Point out each leukocyte.
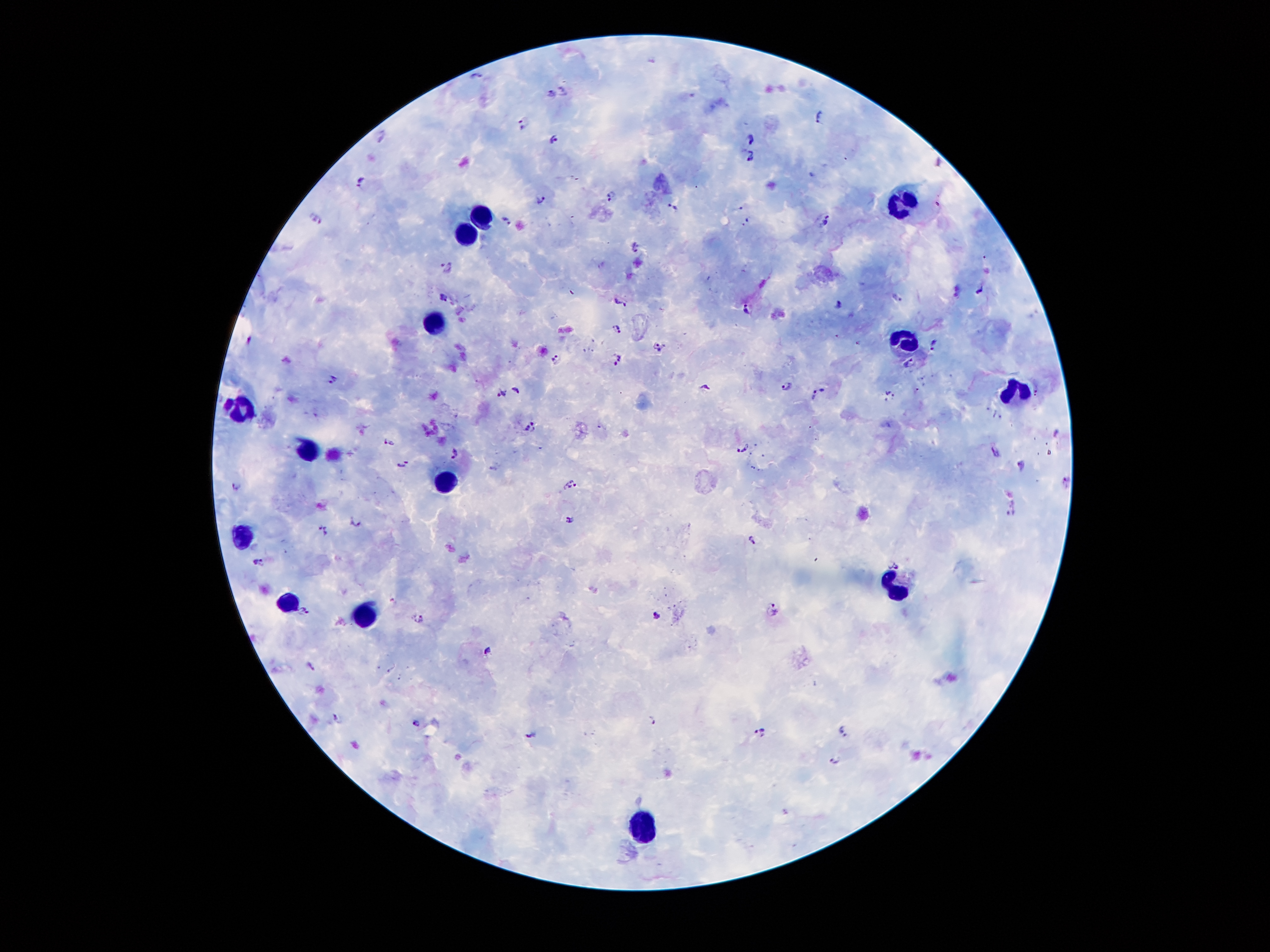
Approximate centers as (x, y) in pixels.
Leukocytes: (901, 209), (485, 221), (472, 231), (435, 326), (904, 345), (1019, 393), (240, 411), (308, 449), (442, 484), (243, 541), (902, 589), (293, 604), (367, 615), (651, 822).

Summary:
  - Plasmodium parasite locations: (654, 60), (477, 76), (564, 90), (552, 94), (817, 115), (522, 124), (381, 133), (750, 138), (553, 139), (751, 155), (359, 182), (612, 195), (540, 200), (672, 207), (739, 210), (507, 220), (316, 221), (826, 221), (745, 224), (635, 247), (447, 266), (978, 290), (572, 292), (443, 297), (898, 297), (620, 302), (838, 305), (746, 309), (618, 329), (837, 336), (250, 339), (859, 343), (934, 344), (658, 347), (618, 358), (556, 359), (910, 364), (333, 379), (786, 386), (707, 387), (515, 389), (499, 392), (817, 393), (890, 397), (531, 427), (1057, 433), (388, 443), (743, 448), (997, 453), (454, 454), (404, 463), (1022, 464), (1066, 480), (571, 485), (235, 486), (1011, 511), (569, 518), (355, 522), (324, 530), (751, 540), (260, 565), (773, 609), (304, 612), (656, 616), (419, 619), (488, 651), (311, 666), (338, 718), (651, 719), (416, 723), (759, 731), (842, 731), (531, 735), (836, 759)
  - Image size: 1270×952 pixels
  - Preparation: thick blood film
  - Field of view: single
  - Stain: Giemsa
  - Magnification: 100x
  - Capture: smartphone through the microscope eyepiece
  - Patient malaria status: positive for Plasmodium falciparum